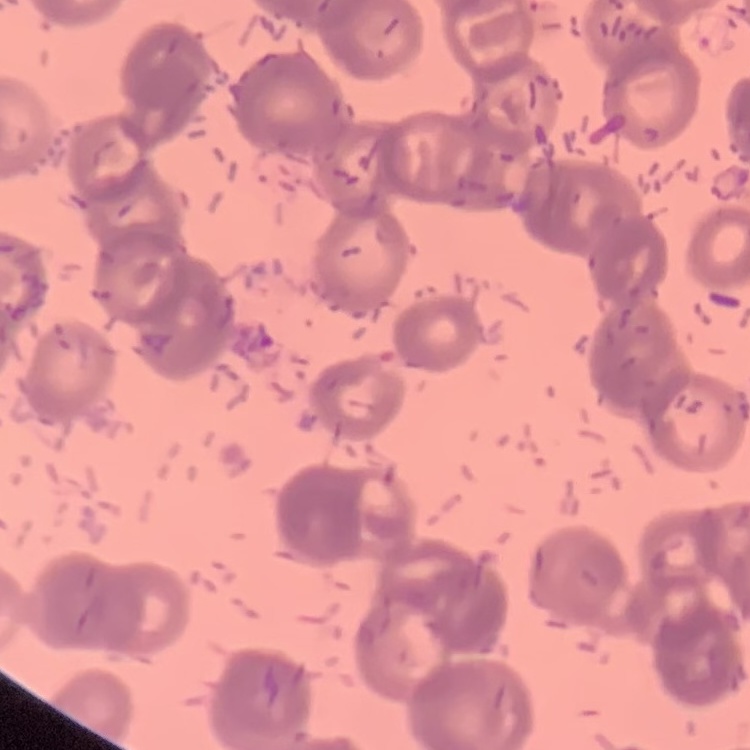 The erythrocytes exhibit rouleaux formation. Square crop of a larger photomicrograph. Field's or Giemsa stain. Thin blood film.